Name the parasite shown.
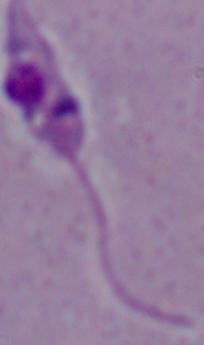
Leishmania.

modality: photomicrograph
magnification: 1000x